Identify the blood parasite species.
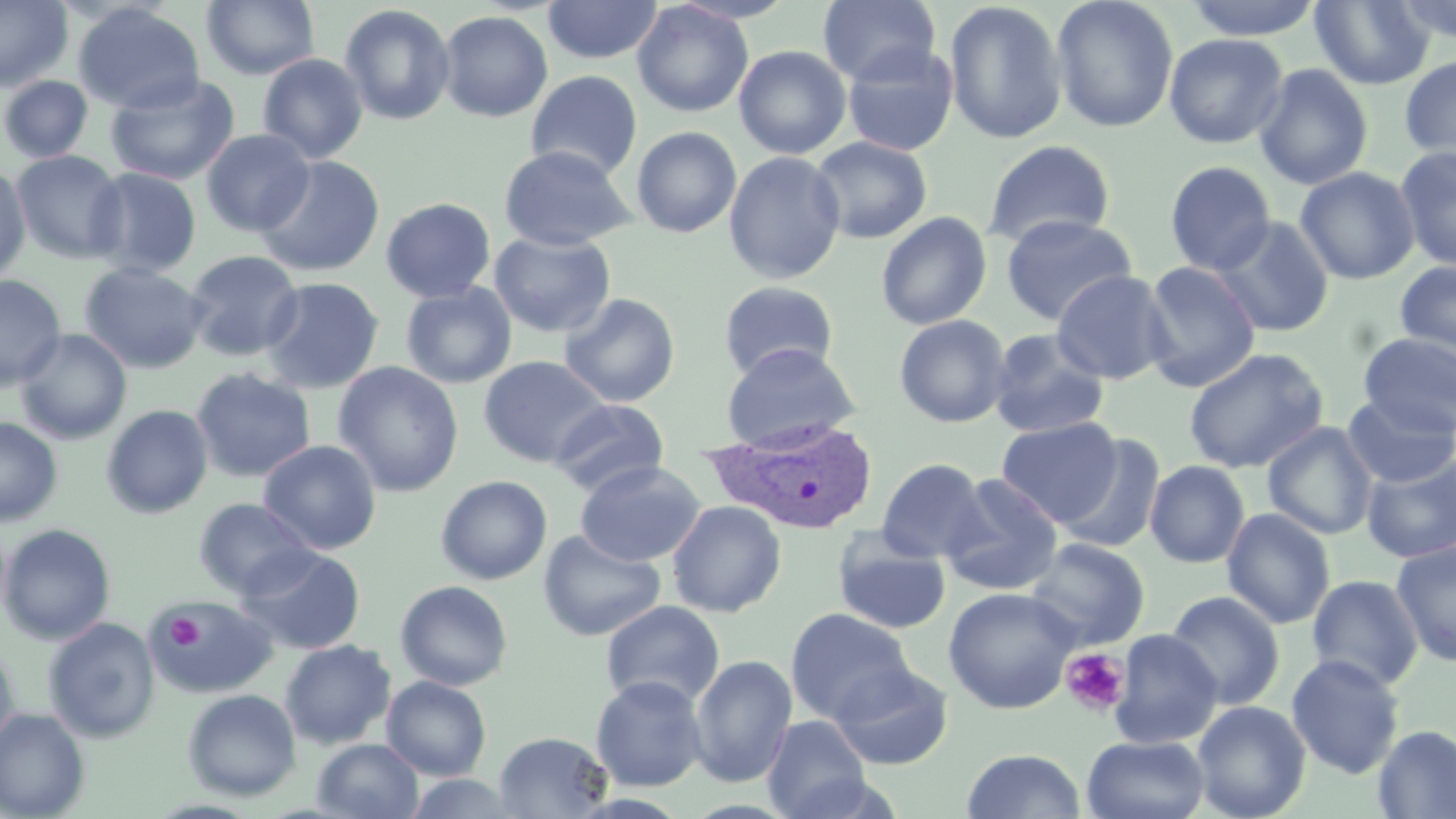
Plasmodium vivax.

Approximate bounding boxes as named x1/y1/x2/y2 corners in pixels. Platelet locations: (x1=164, y1=613, x2=204, y2=652), (x1=1060, y1=647, x2=1131, y2=717). Plasmodium vivax-infected red blood cell locations: (x1=701, y1=418, x2=883, y2=535). Uninfected red blood cell locations: (x1=0, y1=0, x2=73, y2=93), (x1=818, y1=0, x2=941, y2=87), (x1=1050, y1=0, x2=1179, y2=133), (x1=1181, y1=0, x2=1326, y2=40), (x1=1392, y1=0, x2=1456, y2=43), (x1=201, y1=1, x2=321, y2=81), (x1=542, y1=1, x2=663, y2=64), (x1=631, y1=1, x2=754, y2=118), (x1=943, y1=1, x2=1068, y2=144), (x1=1310, y1=1, x2=1435, y2=89), (x1=72, y1=3, x2=205, y2=115), (x1=338, y1=4, x2=455, y2=126), (x1=437, y1=11, x2=553, y2=123), (x1=1163, y1=32, x2=1288, y2=149), (x1=842, y1=44, x2=959, y2=157), (x1=733, y1=45, x2=851, y2=159), (x1=258, y1=53, x2=369, y2=164), (x1=1399, y1=55, x2=1456, y2=167), (x1=1253, y1=64, x2=1374, y2=190), (x1=525, y1=70, x2=643, y2=181), (x1=104, y1=73, x2=239, y2=186), (x1=1, y1=75, x2=93, y2=163), (x1=631, y1=126, x2=742, y2=238), (x1=200, y1=129, x2=315, y2=237), (x1=809, y1=136, x2=932, y2=244), (x1=982, y1=139, x2=1116, y2=249), (x1=498, y1=144, x2=636, y2=250), (x1=1396, y1=144, x2=1456, y2=274), (x1=10, y1=149, x2=127, y2=265), (x1=723, y1=151, x2=846, y2=284), (x1=254, y1=155, x2=386, y2=278), (x1=1164, y1=160, x2=1277, y2=275), (x1=0, y1=166, x2=31, y2=283), (x1=1295, y1=166, x2=1420, y2=285), (x1=85, y1=167, x2=202, y2=278), (x1=381, y1=197, x2=496, y2=303), (x1=876, y1=211, x2=992, y2=330), (x1=1000, y1=214, x2=1136, y2=326), (x1=1212, y1=216, x2=1335, y2=337), (x1=489, y1=230, x2=616, y2=338), (x1=184, y1=250, x2=304, y2=361), (x1=1394, y1=259, x2=1456, y2=365), (x1=1140, y1=261, x2=1261, y2=393), (x1=78, y1=263, x2=208, y2=374), (x1=1051, y1=270, x2=1173, y2=384), (x1=0, y1=275, x2=66, y2=391), (x1=259, y1=277, x2=384, y2=395), (x1=718, y1=281, x2=839, y2=380), (x1=401, y1=283, x2=517, y2=389), (x1=559, y1=292, x2=681, y2=408), (x1=894, y1=314, x2=1011, y2=428), (x1=15, y1=328, x2=132, y2=445), (x1=987, y1=328, x2=1110, y2=439), (x1=1358, y1=333, x2=1456, y2=437), (x1=721, y1=342, x2=861, y2=452), (x1=1184, y1=347, x2=1330, y2=473), (x1=478, y1=355, x2=611, y2=468), (x1=332, y1=362, x2=465, y2=497), (x1=191, y1=367, x2=316, y2=483), (x1=1341, y1=393, x2=1456, y2=488), (x1=550, y1=398, x2=670, y2=495), (x1=101, y1=404, x2=213, y2=519), (x1=0, y1=417, x2=62, y2=526), (x1=995, y1=417, x2=1122, y2=525), (x1=1263, y1=422, x2=1378, y2=540), (x1=1056, y1=434, x2=1166, y2=554), (x1=258, y1=439, x2=382, y2=555), (x1=1361, y1=454, x2=1456, y2=563), (x1=877, y1=458, x2=988, y2=563), (x1=575, y1=460, x2=705, y2=566), (x1=1145, y1=460, x2=1251, y2=568), (x1=940, y1=474, x2=1064, y2=596), (x1=435, y1=475, x2=552, y2=584), (x1=193, y1=498, x2=317, y2=600), (x1=667, y1=500, x2=787, y2=617), (x1=1221, y1=508, x2=1336, y2=629), (x1=0, y1=523, x2=116, y2=645), (x1=538, y1=530, x2=666, y2=642), (x1=833, y1=531, x2=951, y2=635), (x1=1024, y1=537, x2=1150, y2=651), (x1=1391, y1=541, x2=1456, y2=667), (x1=236, y1=545, x2=366, y2=655), (x1=1306, y1=574, x2=1423, y2=691), (x1=395, y1=580, x2=513, y2=691), (x1=943, y1=586, x2=1081, y2=714), (x1=1164, y1=591, x2=1285, y2=709), (x1=149, y1=596, x2=279, y2=698), (x1=600, y1=600, x2=725, y2=709), (x1=785, y1=607, x2=915, y2=725), (x1=43, y1=617, x2=160, y2=743), (x1=1109, y1=630, x2=1222, y2=749), (x1=280, y1=639, x2=396, y2=749), (x1=0, y1=641, x2=22, y2=756), (x1=688, y1=654, x2=798, y2=788), (x1=1286, y1=654, x2=1406, y2=779), (x1=827, y1=661, x2=954, y2=769), (x1=590, y1=675, x2=709, y2=792), (x1=381, y1=676, x2=491, y2=781), (x1=182, y1=689, x2=302, y2=801), (x1=1191, y1=700, x2=1311, y2=819), (x1=0, y1=708, x2=90, y2=819), (x1=761, y1=714, x2=872, y2=818), (x1=1373, y1=725, x2=1456, y2=818), (x1=494, y1=731, x2=614, y2=818), (x1=1081, y1=734, x2=1210, y2=819), (x1=311, y1=738, x2=424, y2=819), (x1=961, y1=748, x2=1086, y2=818), (x1=404, y1=772, x2=523, y2=818). 1000x magnification. May-Grünwald-Giemsa stain. Single field of view. Image is 1456×819 pixels. Light microscopy. Thin blood smear.